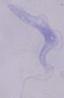 A trypanosome is seen. Micrograph. Captured at 1000x magnification.